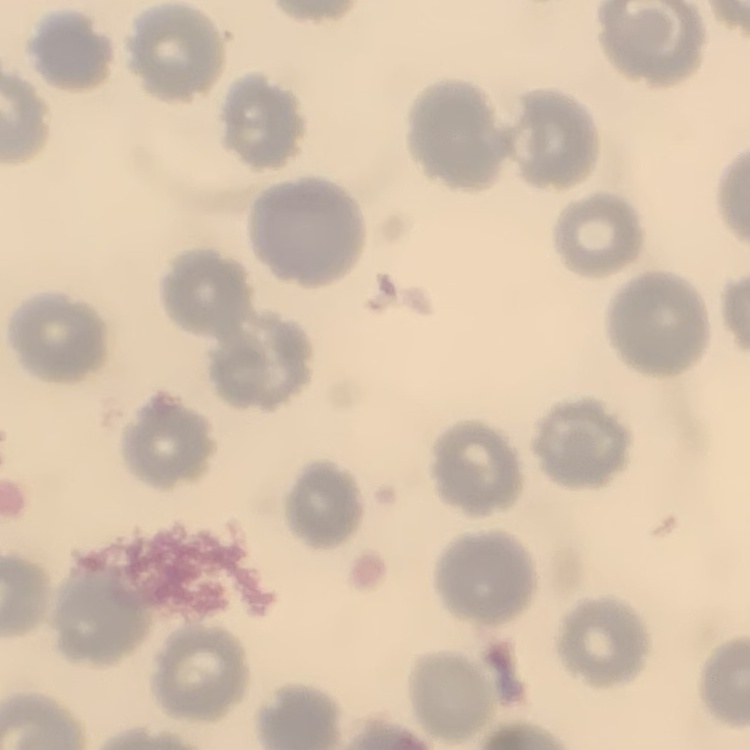
The erythrocytes show no rouleaux formation. Field's or Giemsa stain. One tile cut from a larger photomicrograph. Thin blood smear.